Assess the morphology of the erythrocytes.
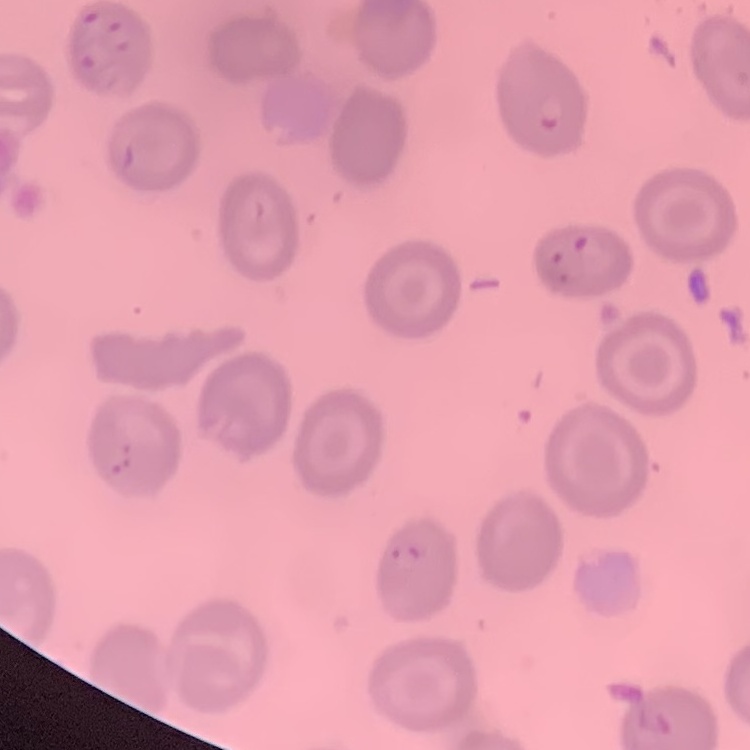

They show no rouleaux formation.

{
  "preparation": "thin blood smear",
  "image_type": "one tile cut from a larger photomicrograph",
  "stain": "Field's or Giemsa"
}